Describe the morphology of the erythrocytes.
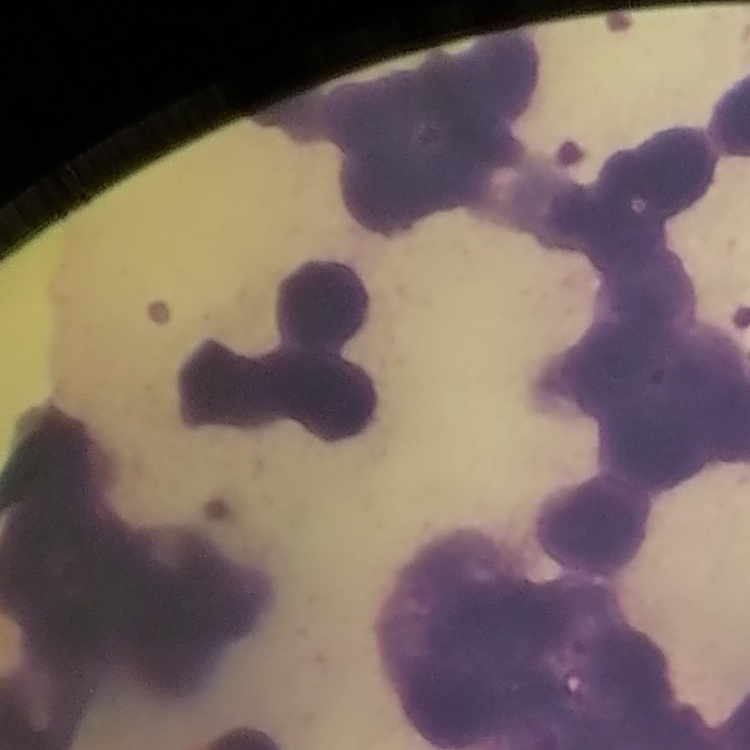
Rouleaux formation.

Thin blood smear. Square crop of a larger photomicrograph. Stained with either Field's or Giemsa.